Evaluate for Plasmodium parasites.
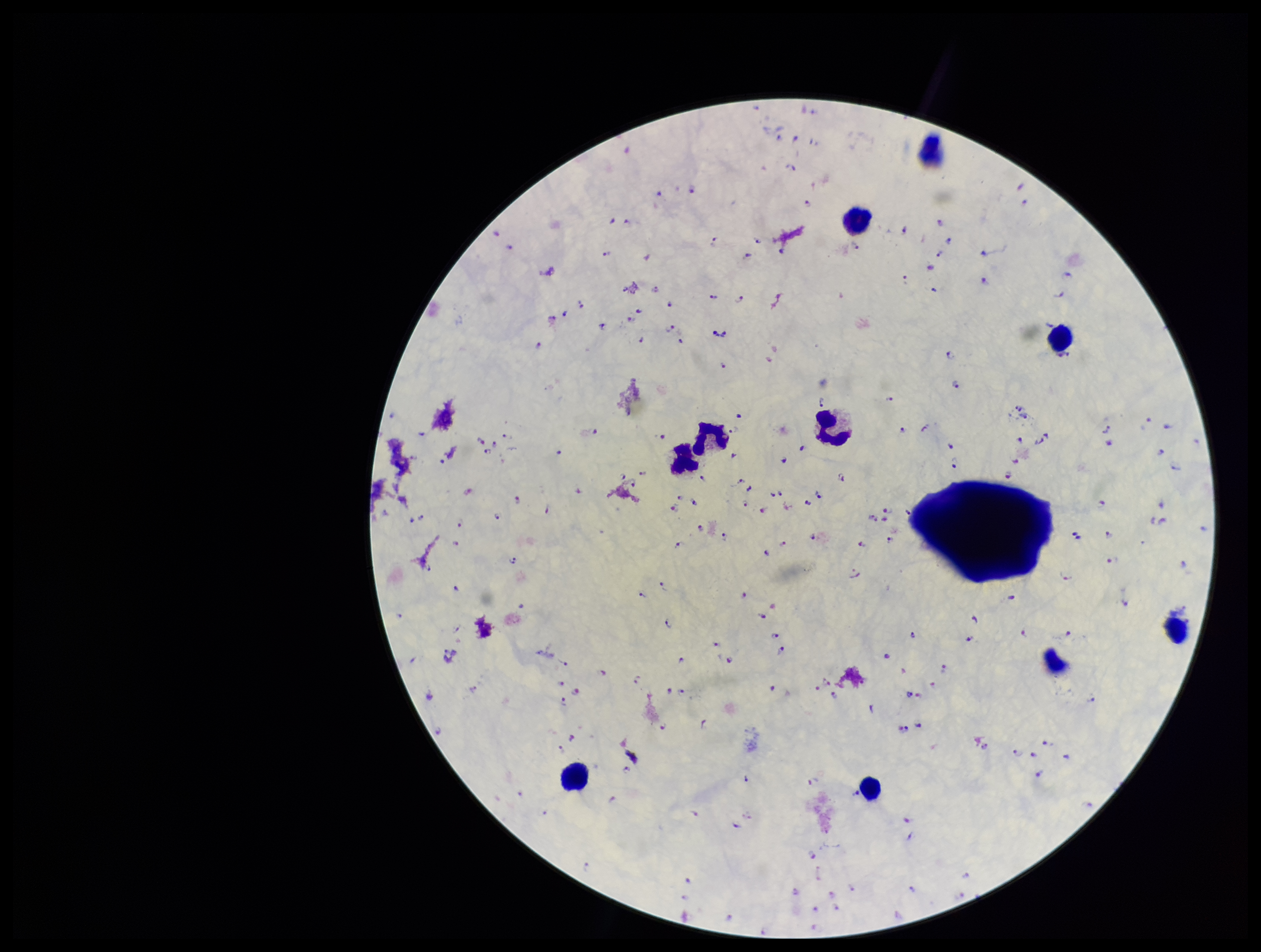
Seen.

field of view = single
species reported for this patient = Plasmodium falciparum
stain = Giemsa
capture = smartphone photograph through the microscope eyepiece
patient malaria status = infected
parasite count = 198
leukocyte count = 9
image size = 1261×952 pixels
preparation = thick blood smear